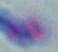
{
  "magnification": "1000x",
  "modality": "photomicrograph",
  "identification": "Toxoplasma gondii"
}